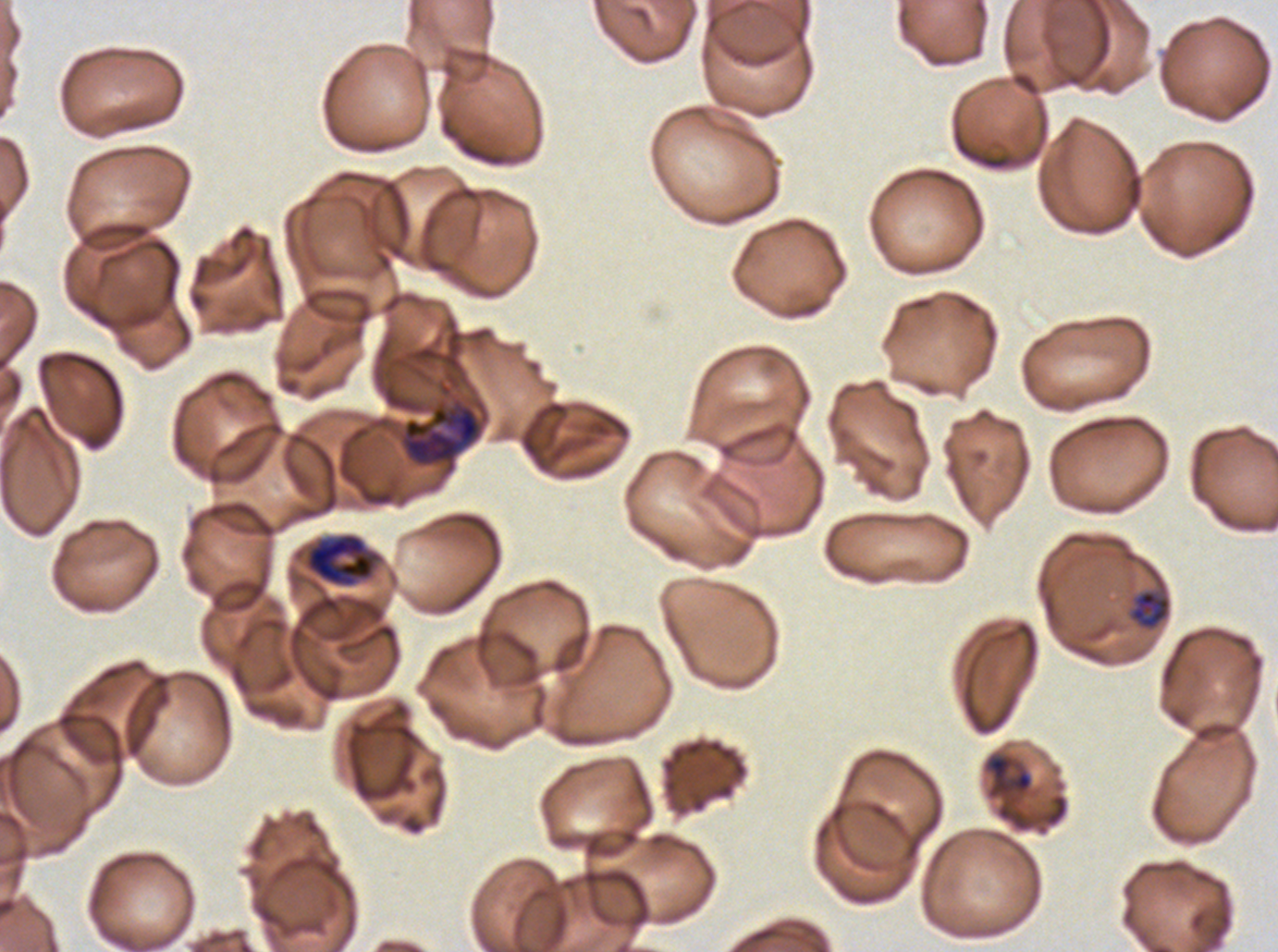

notation = approximate bounding rectangles given as corner coordinates in pixels from the top-left
late-ring/early-trophozoite locations = (x1=1128, y1=589, x2=1172, y2=630), (x1=985, y1=753, x2=1034, y2=799)
early schizont locations = (x1=401, y1=404, x2=482, y2=467), (x1=303, y1=532, x2=382, y2=588)
life-cycle stages observed = late-ring/early-trophozoite, early schizont
preparation = thin blood film
image size = 1278×952 pixels
field of view = one sub-image of a larger composite
stain = Giemsa
specimen = Plasmodium falciparum from a patient in The Gambia, cultured ex vivo for 24 to 48 hours